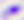
Summary:
  - Magnification: 400x
  - Modality: photomicrograph
  - Identification: Toxoplasma gondii